Identify the parasite.
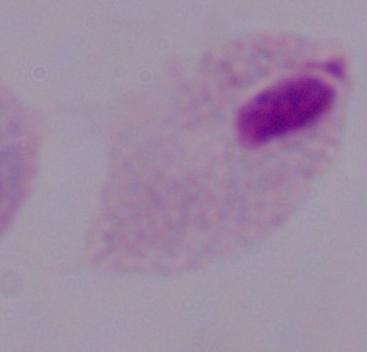

This is a trichomonad.

Summary:
  - Modality: photomicrograph
  - Magnification: 1000x